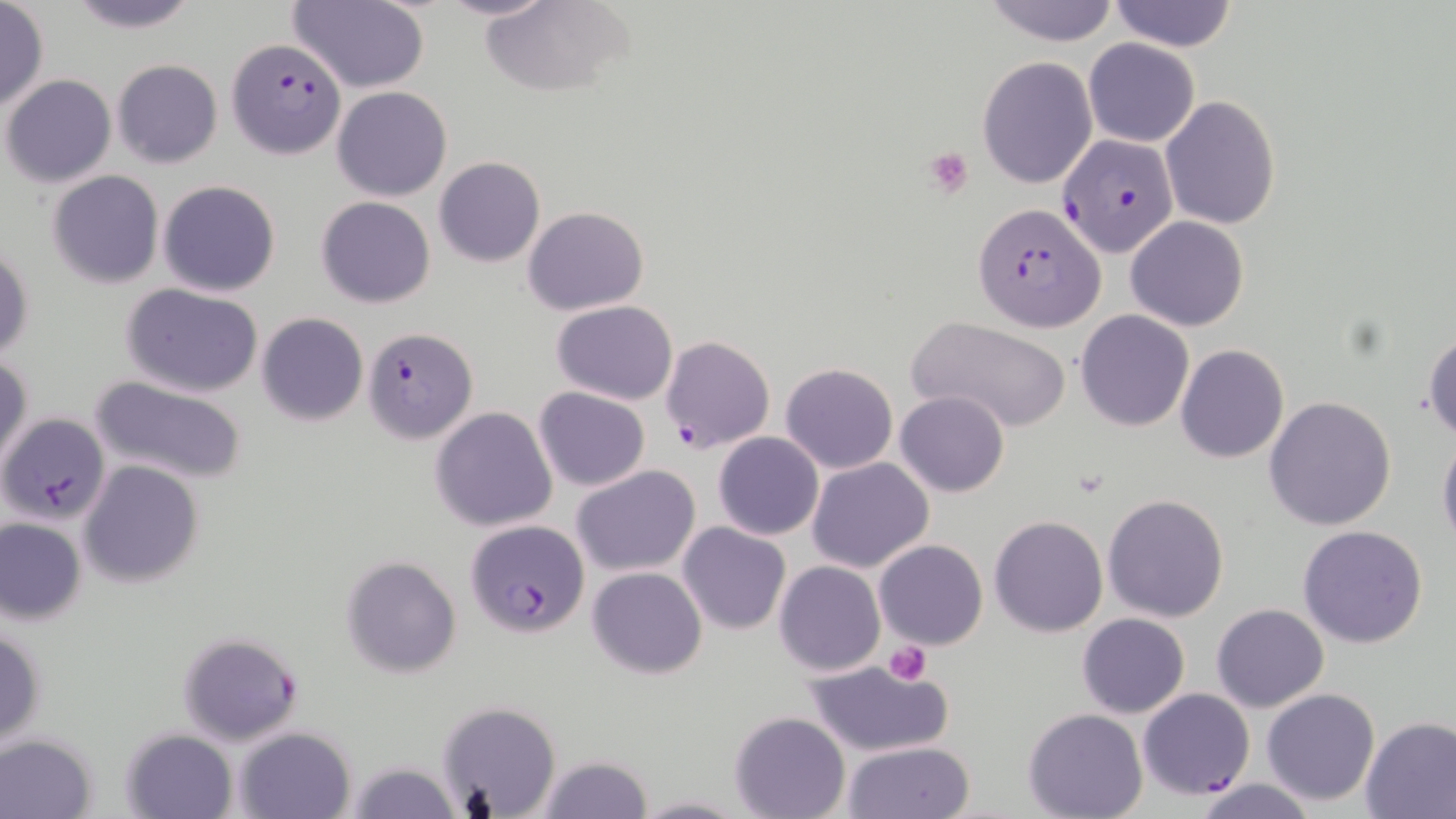
Approximate bounding boxes as (x1,y1)-(x2,y2) corner pairs in pixels. Plasmodium falciparum-infected red blood cell locations: (226,39)-(346,159), (1056,134)-(1178,258), (975,204)-(1105,332), (362,326)-(476,443), (660,335)-(777,454), (1,412)-(110,524), (466,519)-(589,638), (177,631)-(304,744), (1138,688)-(1256,800). Platelet locations: (923,145)-(976,197), (882,640)-(932,685). Uninfected red blood cell locations: (62,0)-(205,33), (438,0)-(554,23), (480,0)-(635,97), (982,0)-(1121,45), (1107,0)-(1239,52), (287,1)-(430,92), (0,3)-(47,109), (1082,37)-(1199,147), (978,55)-(1097,189), (111,59)-(223,169), (2,75)-(116,189), (332,86)-(453,201), (1160,96)-(1282,229), (435,156)-(546,267), (47,171)-(164,289), (157,180)-(282,298), (316,195)-(436,308), (523,205)-(649,314), (1125,216)-(1249,331), (1,244)-(33,363), (121,283)-(265,398), (551,300)-(679,404), (1076,311)-(1194,431), (255,313)-(369,426), (907,316)-(1074,435), (1423,326)-(1456,441), (1175,344)-(1289,464), (0,352)-(32,472), (781,362)-(897,473), (90,376)-(248,486), (534,387)-(650,490), (896,391)-(1009,496), (1264,396)-(1397,531), (431,406)-(558,532), (714,432)-(823,540), (1437,432)-(1456,554), (806,458)-(932,573), (79,460)-(204,588), (572,465)-(700,577), (1102,493)-(1230,622), (990,516)-(1108,637), (0,517)-(87,625), (678,523)-(790,635), (1298,525)-(1429,648), (873,539)-(988,649), (341,555)-(461,678), (774,560)-(885,676), (587,567)-(707,678), (1211,603)-(1328,713), (1078,613)-(1189,719), (0,627)-(46,749), (803,660)-(957,758), (1261,688)-(1381,807), (435,701)-(560,817), (1023,707)-(1147,819), (730,710)-(850,819), (1360,715)-(1456,818), (120,727)-(237,819), (236,727)-(356,819), (0,733)-(97,818), (842,742)-(976,819), (533,754)-(655,819), (345,761)-(461,819), (1192,778)-(1317,819), (634,794)-(744,818). Slide-level diagnosis: Plasmodium falciparum. Captured at 1000x magnification. Light microscopy. May-Grünwald-Giemsa-stained preparation. Image is 1456×819 pixels. Single field of view. Thin blood film.